Name the parasite shown.
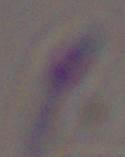

Toxoplasma gondii.

Summary:
  - Modality: micrograph
  - Magnification: 1000x